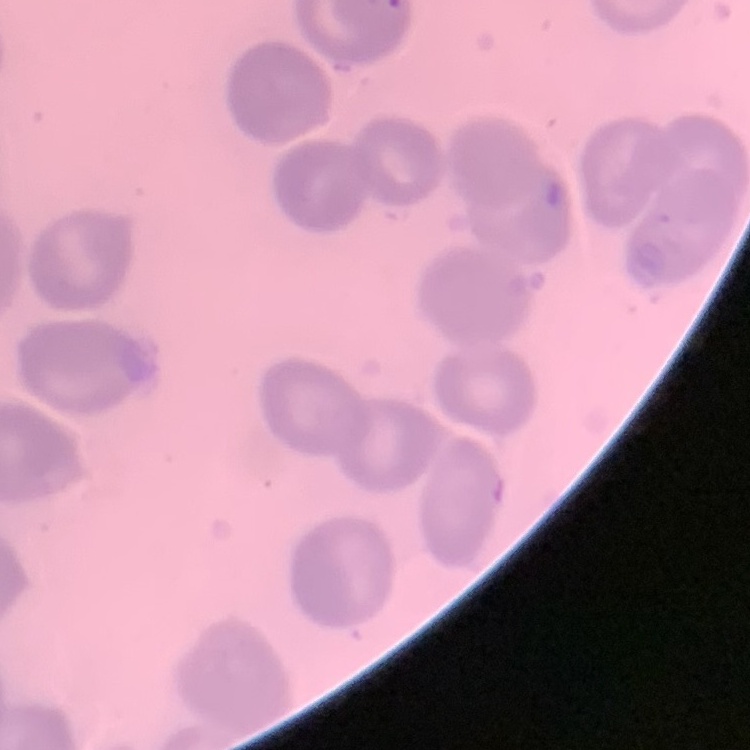

The red blood cells show no rouleaux formation. Square crop of a larger photomicrograph. Thin blood smear. Stained with either Field's or Giemsa.